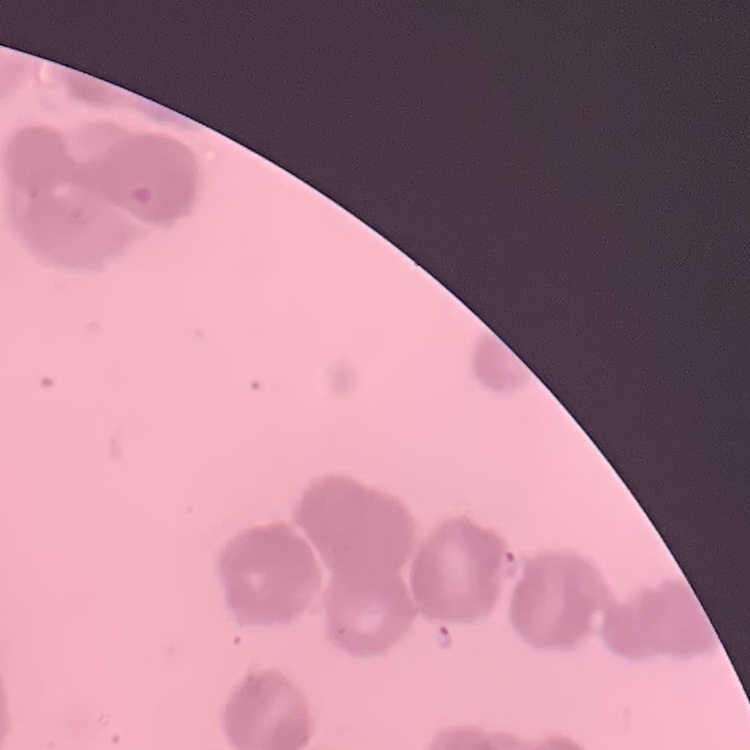 The erythrocytes exhibit rouleaux formation. Thin blood smear. Field's or Giemsa stain. Square crop of a larger photomicrograph.